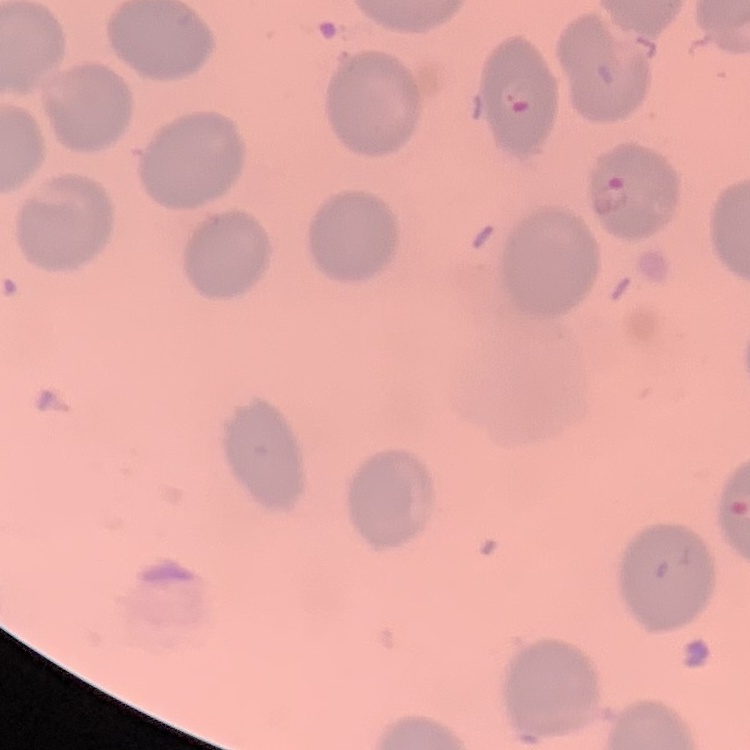

Summary:
  - Erythrocyte morphology: no rouleaux formation
  - Stain: Field's or Giemsa
  - Preparation: thin peripheral smear
  - Image type: square crop of a larger photomicrograph